Classify this cell by malaria status.
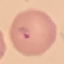

It is parasitized.

image type = cell patch, automatically extracted from a larger field of view and resized to 64 × 64 pixels
capture = smartphone camera at the microscope eyepiece
preparation = thin blood smear
stain = Giemsa